Locate and identify every blood parasite.
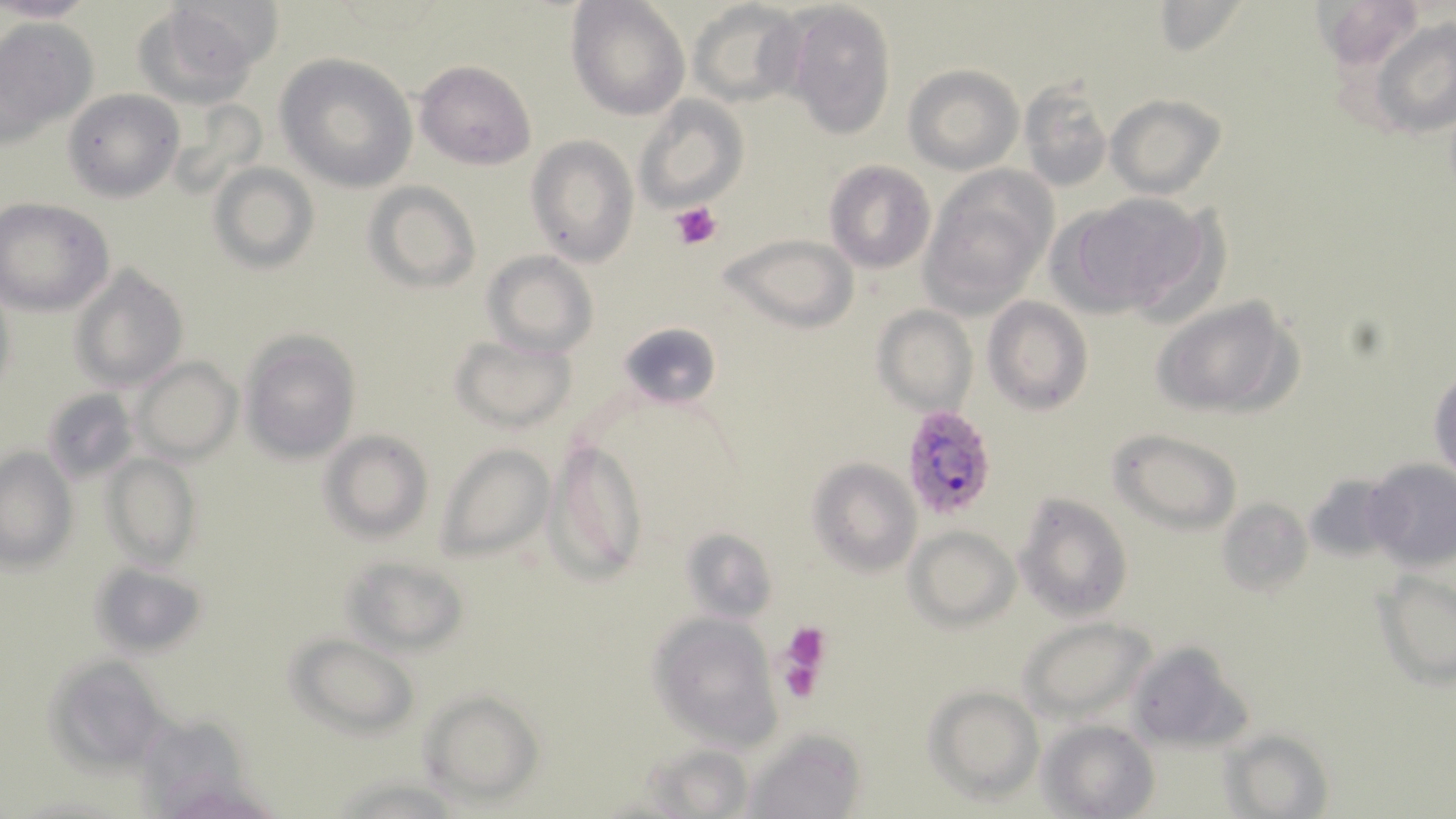
Approximate bounding boxes as (x1,y1)-(x2,y2) corner pairs in pixels.
Plasmodium falciparum-infected red blood cells: (902,403)-(998,520).
No Plasmodium ovale, Plasmodium malariae, Plasmodium vivax, Babesia divergens, or Trypanosoma brucei observed.

Summary:
  - Uninfected red blood cell locations: (1,0)-(98,24), (567,0)-(689,119), (788,1)-(896,142), (690,2)-(807,109), (1150,2)-(1247,59), (134,3)-(267,108), (1368,14)-(1455,138), (0,18)-(97,146), (276,53)-(418,193), (415,60)-(537,170), (905,65)-(1021,173), (1018,78)-(1115,194), (62,88)-(183,202), (633,95)-(749,212), (1106,95)-(1225,198), (525,136)-(639,268), (824,160)-(936,272), (210,162)-(319,272), (922,169)-(1055,313), (365,183)-(481,294), (1059,191)-(1214,320), (2,199)-(116,316), (719,233)-(856,332), (483,251)-(598,358), (72,263)-(188,391), (1151,295)-(1301,420), (982,297)-(1093,416), (874,304)-(976,414), (619,320)-(720,409), (241,330)-(361,462), (449,333)-(577,432), (133,357)-(242,462), (1428,365)-(1456,484), (43,387)-(138,484), (320,430)-(433,541), (1111,430)-(1242,530), (546,438)-(645,578), (438,443)-(555,561), (1,447)-(76,570), (105,453)-(200,568), (808,457)-(922,575), (1362,461)-(1456,572), (1014,492)-(1133,621), (1216,497)-(1312,598), (905,526)-(1020,630), (679,528)-(777,624), (342,553)-(471,654), (88,560)-(207,659), (1373,565)-(1456,688), (652,612)-(782,743), (1018,616)-(1153,721), (287,634)-(418,738), (1127,642)-(1252,753), (48,655)-(176,769), (923,684)-(1044,803), (420,690)-(543,803), (1039,719)-(1158,818), (749,729)-(868,819), (1225,730)-(1333,819), (639,742)-(762,816)
  - Platelet locations: (672,201)-(722,250), (780,621)-(831,691)
  - Slide-level diagnosis: Plasmodium falciparum
  - Magnification: 1000x
  - Preparation: thin blood smear
  - Field of view: single
  - Image size: 1456×819 pixels
  - Modality: optical microscopy
  - Stain: May-Grünwald-Giemsa